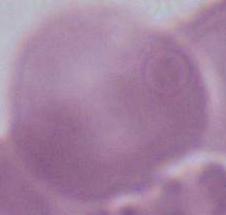 A red blood cell is seen. 1000x magnification. Photomicrograph.